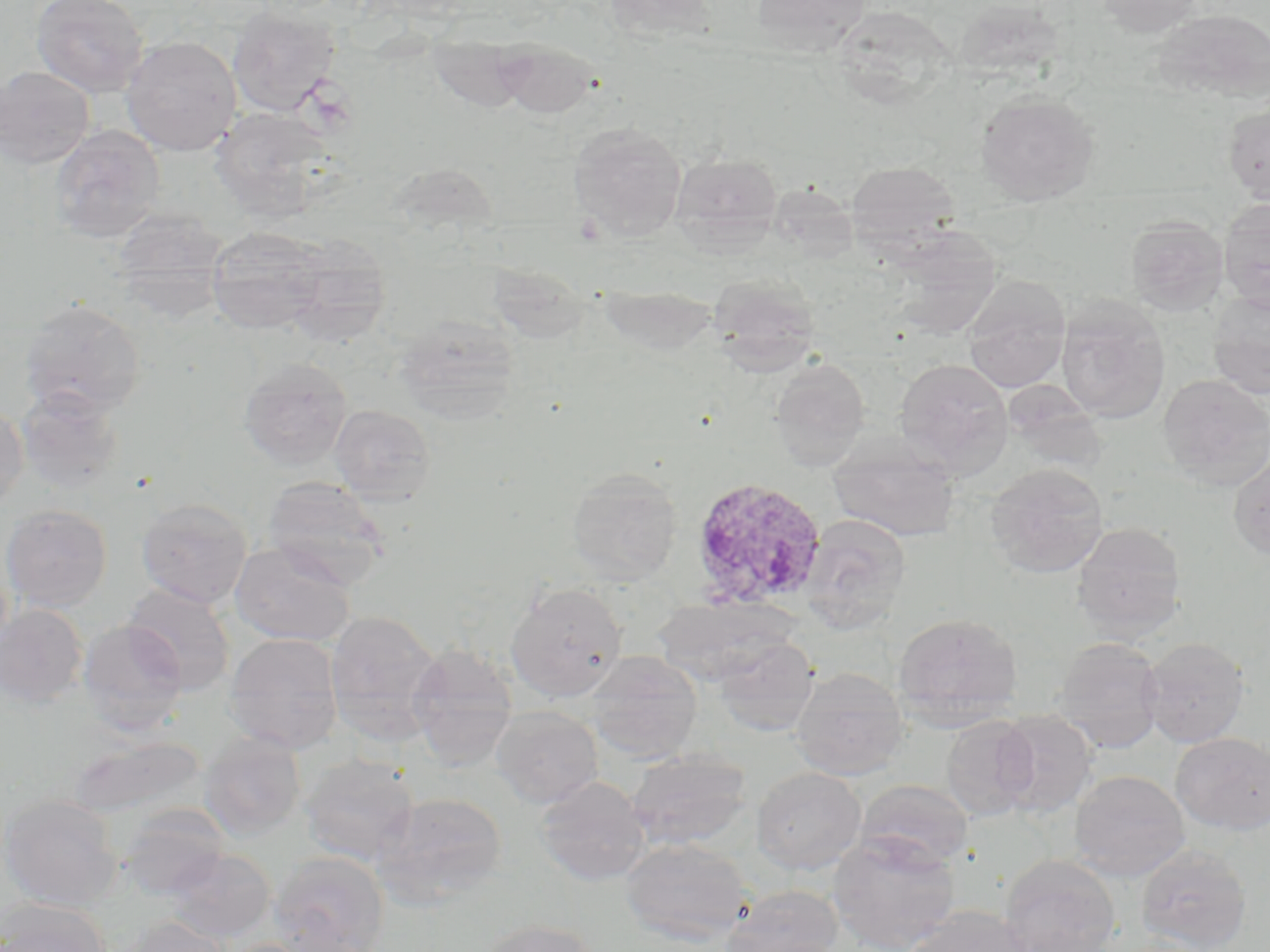
Summary:
  - Coordinate format: approximate bounding boxes as named x1/y1/x2/y2 corners in pixels
  - Plasmodium ovale-infected red blood cell locations: (x1=690, y1=476, x2=828, y2=611)
  - Uninfected red blood cell locations: (x1=30, y1=0, x2=149, y2=98), (x1=603, y1=0, x2=720, y2=43), (x1=751, y1=0, x2=871, y2=54), (x1=1093, y1=0, x2=1206, y2=35), (x1=952, y1=1, x2=1065, y2=85), (x1=226, y1=5, x2=340, y2=117), (x1=1151, y1=9, x2=1270, y2=103), (x1=426, y1=32, x2=534, y2=113), (x1=121, y1=36, x2=241, y2=156), (x1=493, y1=40, x2=601, y2=119), (x1=0, y1=65, x2=95, y2=170), (x1=975, y1=91, x2=1100, y2=205), (x1=1223, y1=101, x2=1270, y2=204), (x1=209, y1=106, x2=336, y2=220), (x1=568, y1=122, x2=687, y2=241), (x1=49, y1=125, x2=165, y2=244), (x1=669, y1=152, x2=783, y2=252), (x1=844, y1=161, x2=961, y2=250), (x1=1218, y1=196, x2=1270, y2=313), (x1=110, y1=206, x2=231, y2=313), (x1=1125, y1=215, x2=1229, y2=316), (x1=205, y1=226, x2=327, y2=335), (x1=884, y1=229, x2=1003, y2=340), (x1=279, y1=238, x2=393, y2=347), (x1=708, y1=275, x2=822, y2=372), (x1=962, y1=277, x2=1071, y2=393), (x1=1207, y1=291, x2=1270, y2=400), (x1=1056, y1=297, x2=1171, y2=423), (x1=18, y1=298, x2=147, y2=417), (x1=394, y1=314, x2=521, y2=423), (x1=239, y1=357, x2=353, y2=470), (x1=894, y1=357, x2=1013, y2=476), (x1=769, y1=359, x2=870, y2=470), (x1=1157, y1=372, x2=1270, y2=489), (x1=15, y1=385, x2=125, y2=494), (x1=0, y1=401, x2=28, y2=511), (x1=329, y1=404, x2=437, y2=504), (x1=828, y1=432, x2=959, y2=543), (x1=1228, y1=450, x2=1270, y2=560), (x1=985, y1=463, x2=1108, y2=579), (x1=566, y1=467, x2=682, y2=584), (x1=262, y1=476, x2=392, y2=588), (x1=136, y1=498, x2=252, y2=608), (x1=0, y1=504, x2=112, y2=611), (x1=801, y1=514, x2=911, y2=633), (x1=1071, y1=522, x2=1186, y2=640), (x1=229, y1=540, x2=355, y2=647), (x1=505, y1=581, x2=627, y2=702), (x1=122, y1=583, x2=235, y2=695), (x1=655, y1=596, x2=792, y2=685), (x1=0, y1=604, x2=88, y2=708), (x1=324, y1=609, x2=443, y2=743), (x1=893, y1=612, x2=1024, y2=724), (x1=78, y1=620, x2=188, y2=736), (x1=224, y1=632, x2=344, y2=754), (x1=713, y1=634, x2=819, y2=736), (x1=1052, y1=637, x2=1166, y2=754), (x1=1139, y1=637, x2=1250, y2=748), (x1=406, y1=643, x2=518, y2=768), (x1=587, y1=651, x2=702, y2=762), (x1=790, y1=666, x2=908, y2=781), (x1=491, y1=706, x2=603, y2=808), (x1=993, y1=710, x2=1098, y2=819), (x1=940, y1=715, x2=1039, y2=820), (x1=1170, y1=731, x2=1270, y2=835), (x1=199, y1=733, x2=307, y2=840), (x1=66, y1=735, x2=207, y2=819), (x1=626, y1=750, x2=751, y2=852), (x1=299, y1=752, x2=419, y2=865), (x1=751, y1=767, x2=866, y2=875), (x1=1070, y1=769, x2=1189, y2=880), (x1=536, y1=776, x2=650, y2=886), (x1=856, y1=779, x2=974, y2=871), (x1=374, y1=791, x2=508, y2=906), (x1=0, y1=795, x2=122, y2=910), (x1=117, y1=803, x2=232, y2=900), (x1=828, y1=833, x2=961, y2=952), (x1=620, y1=837, x2=754, y2=946), (x1=1136, y1=843, x2=1252, y2=951), (x1=164, y1=848, x2=275, y2=942), (x1=270, y1=851, x2=390, y2=952), (x1=999, y1=854, x2=1121, y2=952), (x1=722, y1=885, x2=843, y2=952), (x1=0, y1=902, x2=111, y2=952), (x1=900, y1=905, x2=1035, y2=952), (x1=122, y1=914, x2=233, y2=952), (x1=478, y1=918, x2=600, y2=952)
  - Slide-level diagnosis: Plasmodium ovale
  - Modality: light microscopy
  - Image size: 1270×952 pixels
  - Magnification: 1000x
  - Stain: May-Grünwald-Giemsa
  - Field of view: one of a larger specimen
  - Preparation: thin blood smear